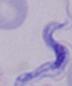
{
  "magnification": "1000x",
  "identification": "trypanosome",
  "modality": "micrograph"
}